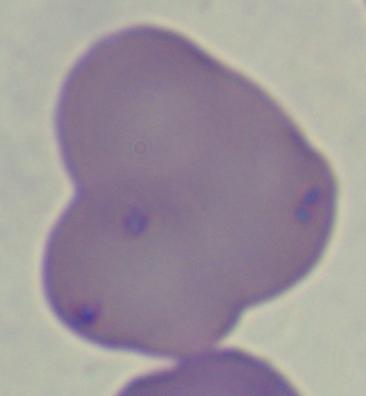
{
  "magnification": "1000x",
  "identification": "Babesia",
  "modality": "micrograph"
}